Comment on the morphology of the erythrocytes.
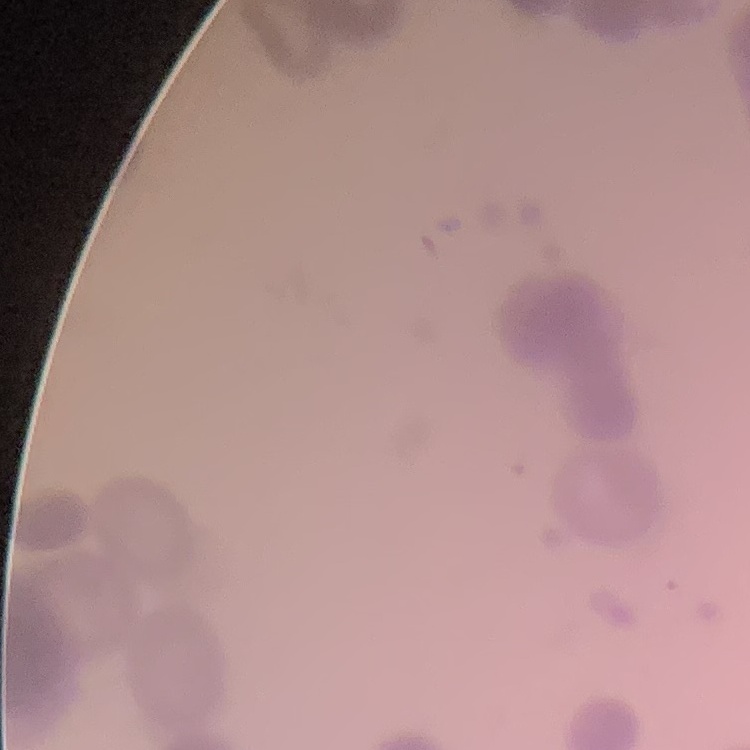
Rouleaux formation.

preparation = thin blood smear
stain = Field's or Giemsa
image type = square crop of a larger photomicrograph